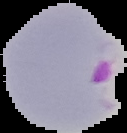

preparation = thin blood smear
image size = 127×133 pixels
malaria status = parasitized
image type = segmented cell region on a black background